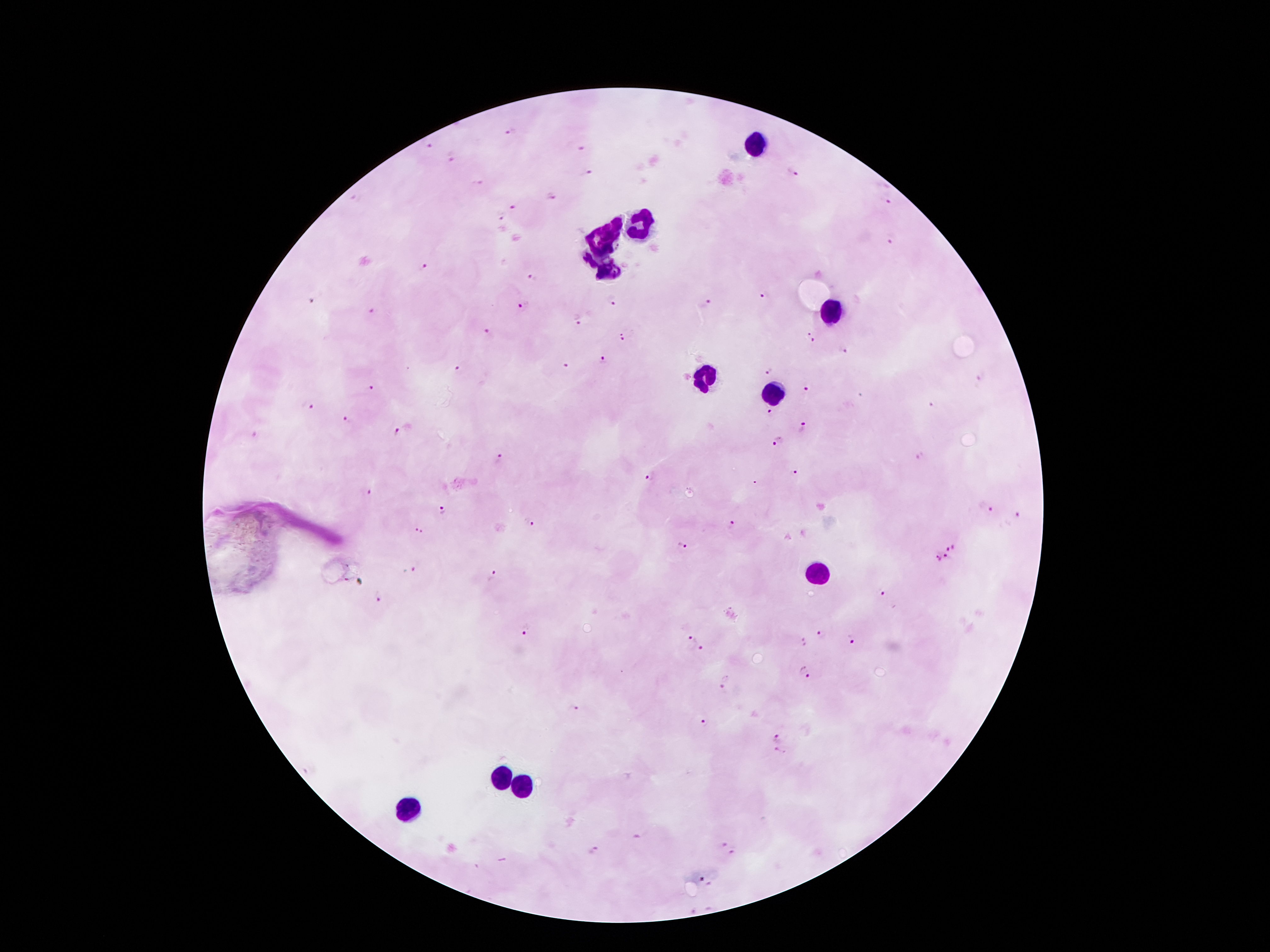

coordinate format = approximate centers as [x, y] in pixels
leukocyte locations = [753, 143], [642, 225], [611, 231], [598, 248], [590, 263], [607, 272], [829, 311], [701, 374], [770, 393], [815, 575], [501, 777], [520, 790], [405, 814]
Plasmodium parasite locations = [512, 132], [429, 146], [579, 148], [451, 156], [793, 172], [590, 173], [477, 183], [553, 197], [889, 201], [516, 205], [499, 214], [889, 238], [425, 266], [532, 277], [764, 296], [610, 300], [311, 302], [706, 303], [523, 305], [370, 312], [577, 320], [488, 333], [623, 338], [811, 338], [843, 352], [603, 361], [567, 366], [458, 370], [769, 372], [980, 378], [806, 386], [372, 389], [933, 405], [307, 406], [770, 412], [346, 420], [804, 428], [395, 431], [255, 436], [778, 441], [919, 457], [498, 461], [796, 471], [650, 477], [365, 493], [987, 508], [443, 509], [1019, 515], [530, 522], [732, 524], [419, 530], [681, 544], [954, 548], [946, 549], [946, 558], [937, 559], [411, 569], [492, 574], [880, 592], [379, 597], [524, 630], [821, 635], [853, 638], [692, 639], [803, 641], [702, 648], [805, 673], [724, 682], [571, 707], [705, 721], [778, 739], [778, 753], [720, 842], [594, 848], [733, 853], [701, 879]
stain = Giemsa
patient malaria status = positive for Plasmodium falciparum
image size = 1270×952 pixels
preparation = thick peripheral-blood smear
capture = smartphone camera through the microscope eyepiece
field of view = one from this slide
magnification = 100x